Assess this cell for malaria.
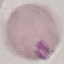
It is uninfected.

Summary:
  - Stain: Giemsa
  - Capture: smartphone through the microscope eyepiece
  - Image type: cell patch, automatically extracted from a larger field of view and resized to 64 × 64 pixels
  - Preparation: thin blood smear